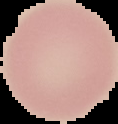
Summary:
  - Image size: 118×124 pixels
  - Preparation: thin blood smear
  - Image type: cell region segmented out of the field of view; surrounding area masked to black
  - Result: no malaria parasites detected